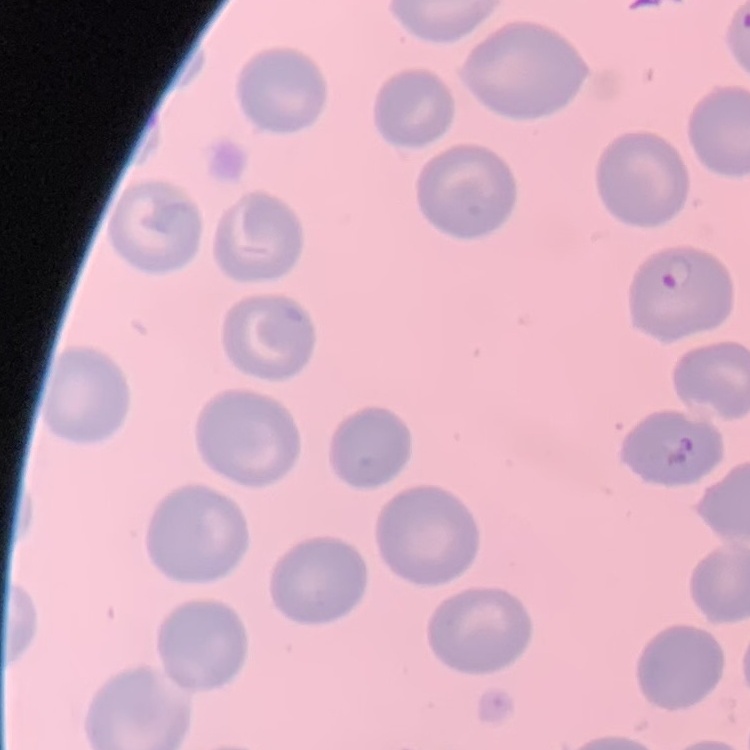
erythrocyte morphology = no rouleaux formation
preparation = thin blood smear
stain = Field's or Giemsa
image type = one tile cut from a larger photomicrograph